Point out malaria parasites and leukocytes.
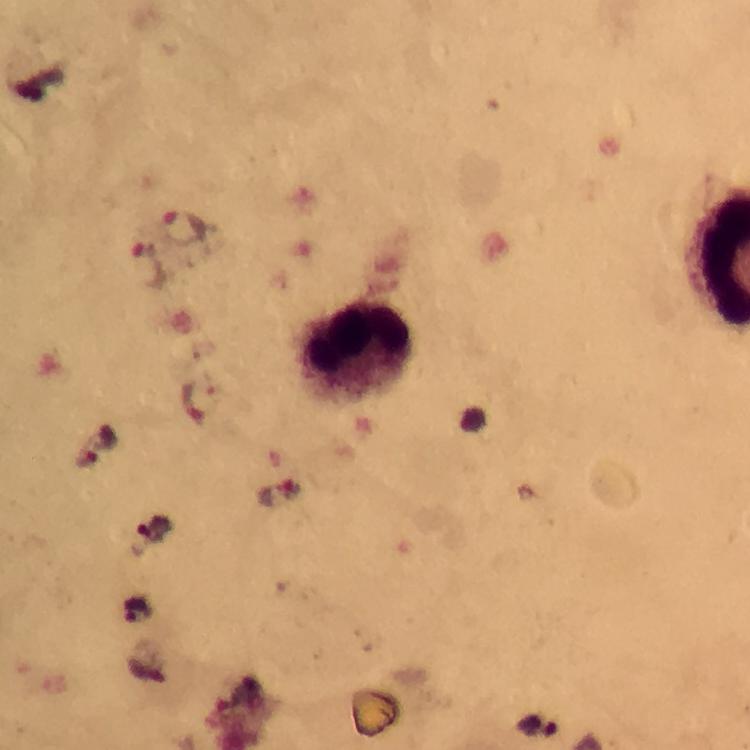
Approximate centers as [x, y] in pixels.
Malaria parasites: [185, 229], [148, 264], [101, 443], [136, 612].
Leukocytes: [358, 348].

{
  "magnification": "100x",
  "image_size": "750×750 pixels",
  "context": "from a diagnostic examination for malaria",
  "stain": "Giemsa",
  "preparation": "thick smear",
  "cropped_from": "a single field of view",
  "immersion_oil": "applied",
  "capture": "smartphone mounted on the microscope"
}